Report the malaria status of this cell.
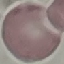
Uninfected.

Giemsa stain. Thin blood film. Cell patch, automatically extracted from a larger field of view and resized to 64 × 64 pixels. Photographed with a smartphone camera at the microscope eyepiece.